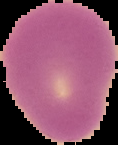
image_size: 118×145 pixels
image_type: cell region segmented out of the field of view; surrounding area masked to black
malaria_status: uninfected
preparation: thin blood film